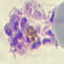
malaria status = parasitized
stain = Giemsa
capture = smartphone camera at the microscope eyepiece
image type = automatically extracted cell patch, resized to 64 × 64 pixels
preparation = thin blood smear